Give the preparation type.
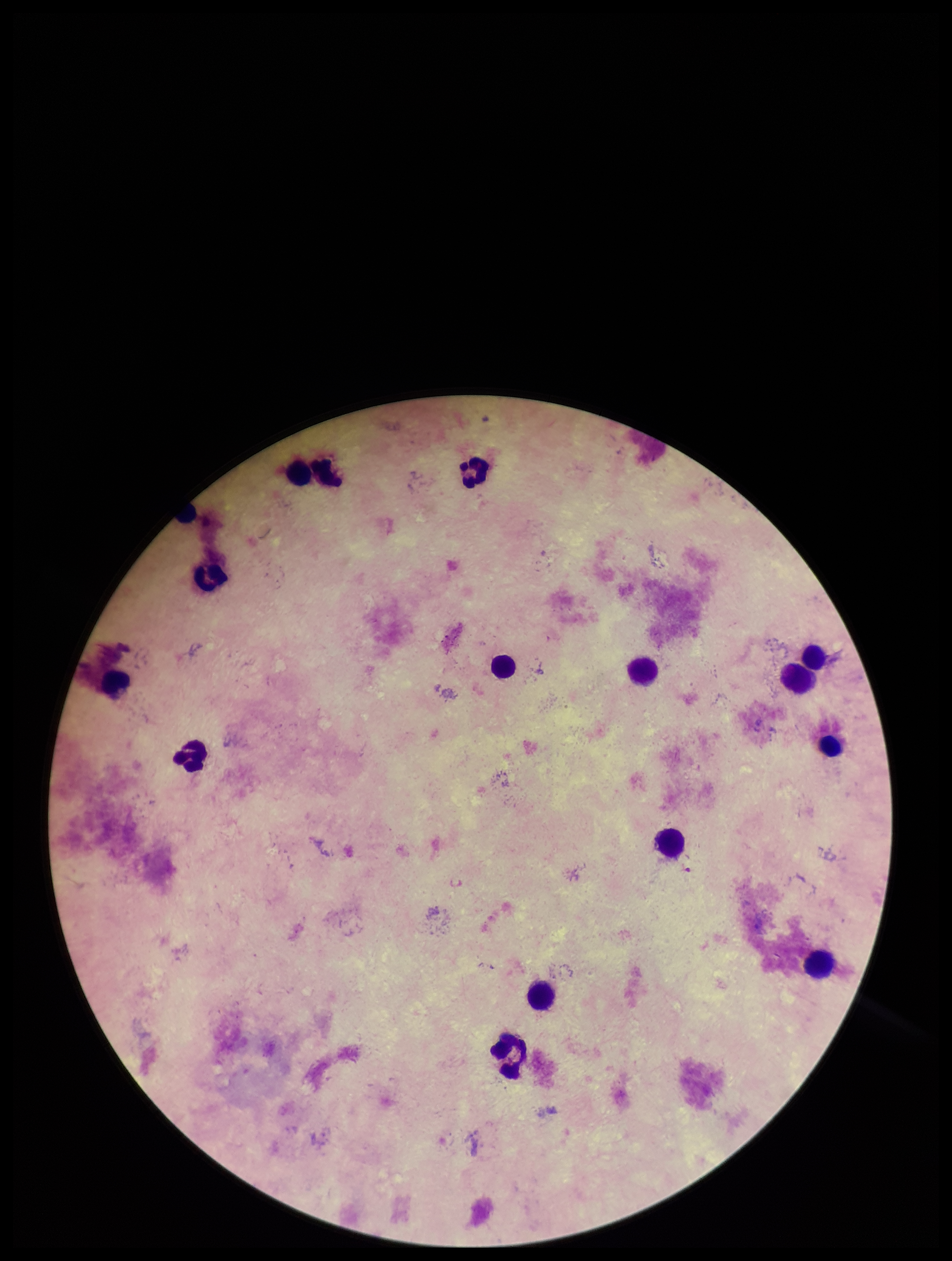

It is a thick blood smear.

stain = Giemsa
Plasmodium parasites = none seen
image size = 952×1261 pixels
parasite count = 0
field of view = one from this slide
patient malaria status = negative
capture = smartphone photograph through the microscope eyepiece
leukocyte count = 15